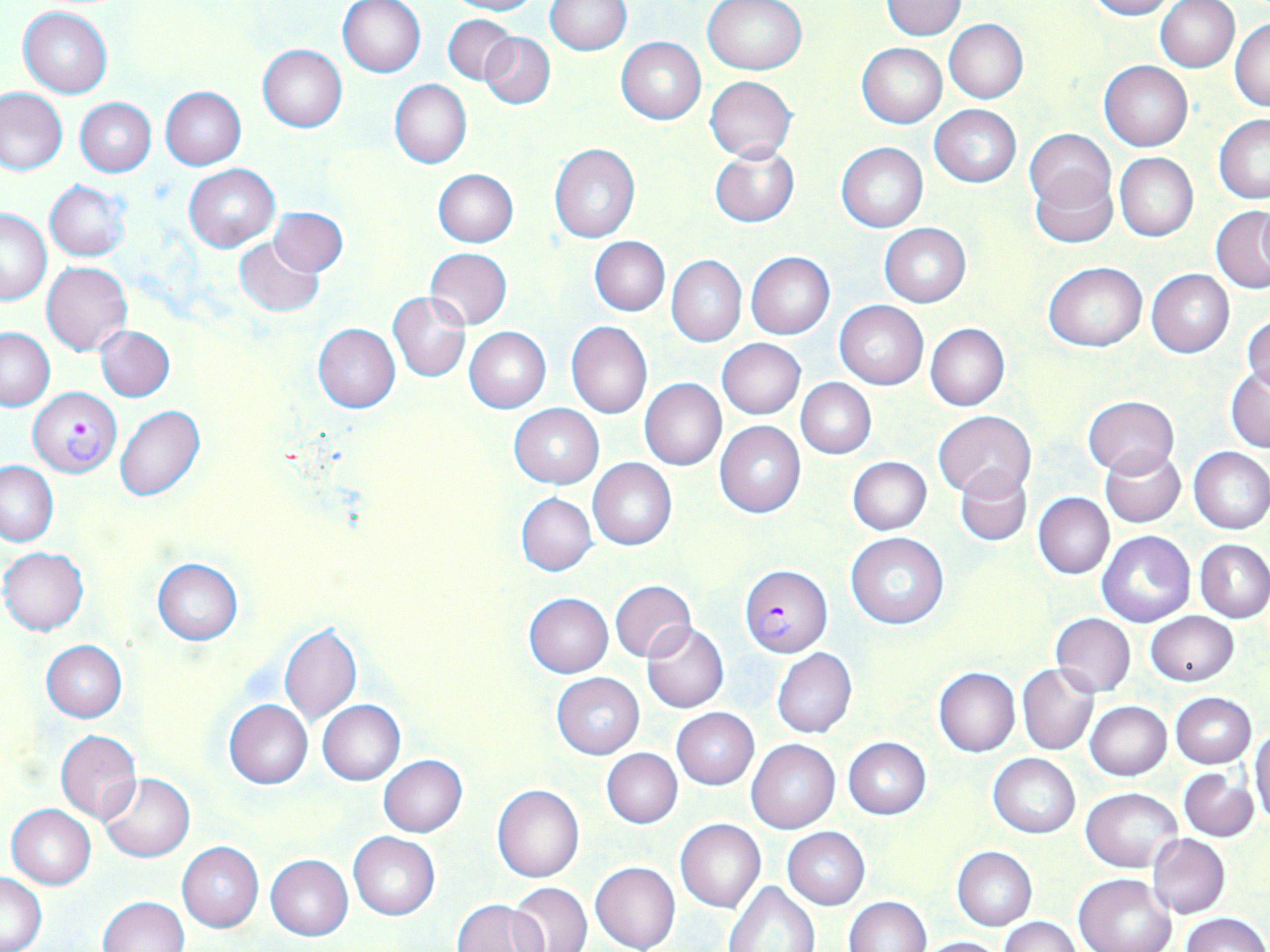 Approximate bounding boxes as (x1,y1)-(x2,y2) corner pairs in pixels. Plasmodium falciparum-infected red blood cell locations: (29,388)-(121,476), (739,564)-(832,657). Uninfected red blood cell locations: (338,0)-(426,78), (445,0)-(544,15), (547,0)-(631,54), (703,0)-(808,75), (1085,0)-(1180,19), (881,1)-(966,39), (1154,1)-(1241,73), (18,6)-(113,98), (443,15)-(517,84), (1230,17)-(1270,113), (944,19)-(1028,103), (480,31)-(555,110), (616,37)-(706,123), (857,43)-(946,128), (258,45)-(347,132), (1100,61)-(1192,151), (705,76)-(796,162), (390,79)-(471,168), (1,87)-(67,175), (160,87)-(246,169), (75,98)-(155,176), (930,104)-(1021,188), (1213,115)-(1270,203), (1025,129)-(1113,213), (836,142)-(928,232), (549,144)-(640,244), (710,144)-(800,227), (1114,153)-(1197,241), (184,165)-(280,250), (433,168)-(517,247), (1029,168)-(1117,248), (45,180)-(130,261), (1210,206)-(1270,294), (270,207)-(347,276), (1,209)-(52,305), (879,222)-(970,307), (234,237)-(325,317), (590,237)-(669,316), (425,248)-(512,329), (745,252)-(834,339), (666,255)-(746,347), (42,261)-(131,356), (1044,263)-(1146,351), (1147,269)-(1235,358), (388,292)-(472,382), (834,300)-(929,389), (1243,313)-(1270,394), (566,321)-(652,418), (313,323)-(400,413), (925,323)-(1009,411), (96,326)-(174,402), (0,327)-(54,411), (464,327)-(551,412), (716,338)-(805,419), (1226,367)-(1270,452), (796,377)-(876,459), (640,378)-(727,471), (1082,396)-(1178,477), (510,403)-(603,487), (115,405)-(206,502), (932,411)-(1035,501), (715,421)-(806,518), (1101,446)-(1186,527), (1188,447)-(1270,535), (848,457)-(932,534), (588,458)-(676,550), (1,460)-(58,545), (955,465)-(1031,546), (1034,492)-(1114,578), (517,493)-(597,576), (1098,530)-(1194,628), (845,531)-(948,630), (1196,539)-(1270,621), (1,547)-(88,635), (152,558)-(242,645), (609,579)-(695,662), (524,592)-(614,678), (1146,611)-(1239,686), (1050,613)-(1135,696), (278,621)-(362,726), (642,621)-(729,712), (41,641)-(127,722), (772,648)-(856,738), (1017,663)-(1099,756), (934,667)-(1020,757), (552,673)-(644,758), (1170,693)-(1256,767), (223,699)-(313,788), (317,699)-(405,785), (1086,701)-(1172,781), (672,708)-(758,789), (1250,726)-(1270,827), (55,730)-(141,823), (843,737)-(930,819), (746,740)-(840,834), (601,748)-(682,828), (989,753)-(1080,838), (378,755)-(468,837), (1179,768)-(1258,842), (98,772)-(195,863), (492,784)-(584,883), (1081,787)-(1183,873), (7,804)-(96,889), (675,818)-(765,913), (782,827)-(870,909), (348,833)-(439,920), (1147,834)-(1229,919), (177,841)-(263,932), (953,847)-(1037,931), (265,854)-(353,941), (589,861)-(680,952), (1,872)-(47,951), (1074,872)-(1175,952), (724,880)-(821,952), (508,882)-(592,952), (844,895)-(931,952), (99,896)-(189,951), (453,899)-(547,951), (1181,912)-(1270,952), (1000,917)-(1083,952), (919,936)-(1004,952). Slide-level diagnosis: Plasmodium falciparum. Thin blood film. Image is 1270×952 pixels. Light microscopy. Single field of view. Captured at 1000x magnification. May-Grünwald-Giemsa-stained preparation.